Identify the parasite.
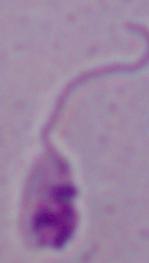

Leishmania.

Captured at 1000x magnification. Photomicrograph.